Assess the morphology of the red blood cells.
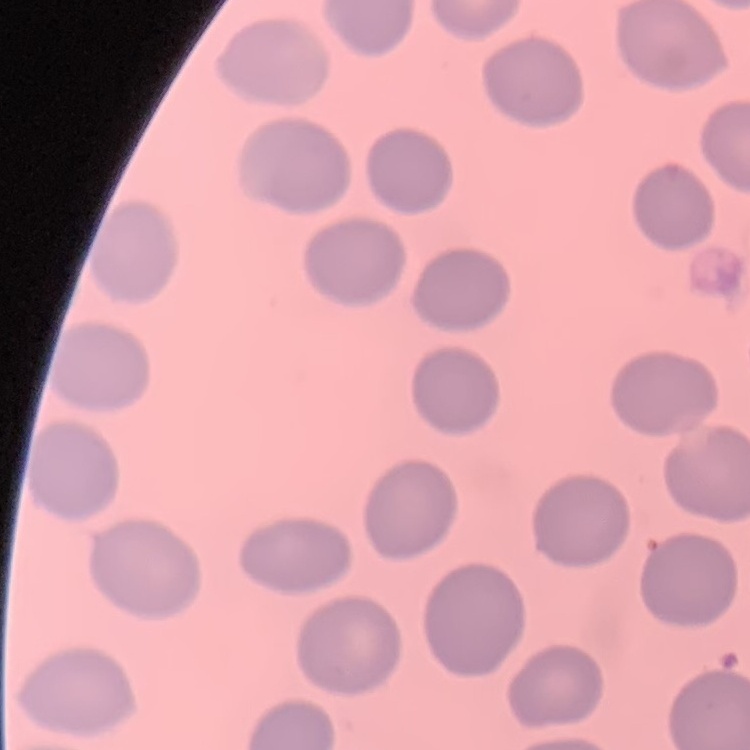
No rouleaux formation.

stain = Field's or Giemsa
preparation = thin blood film
image type = one tile cut from a larger photomicrograph